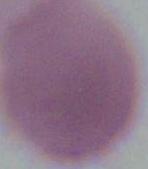

identification: erythrocyte
magnification: 1000x
modality: micrograph